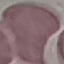
malaria status = uninfected
image type = cell patch, automatically extracted from a larger field of view and resized to 64 × 64 pixels
capture = smartphone camera at the microscope eyepiece
stain = Giemsa
preparation = thin blood film